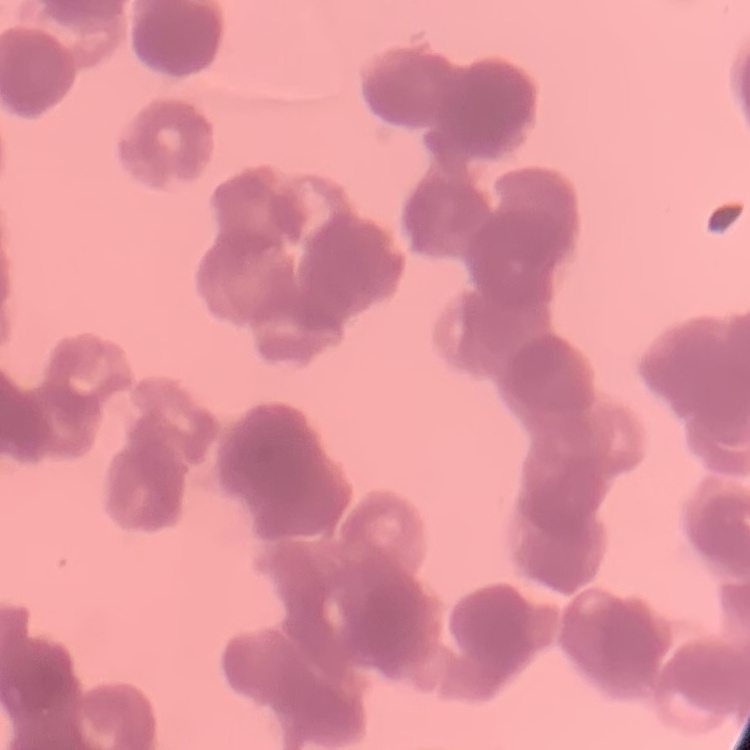
The red blood cells show rouleaux formation. One tile cut from a larger photomicrograph. Thin blood film. Field's or Giemsa stain.